Identify the preparation type.
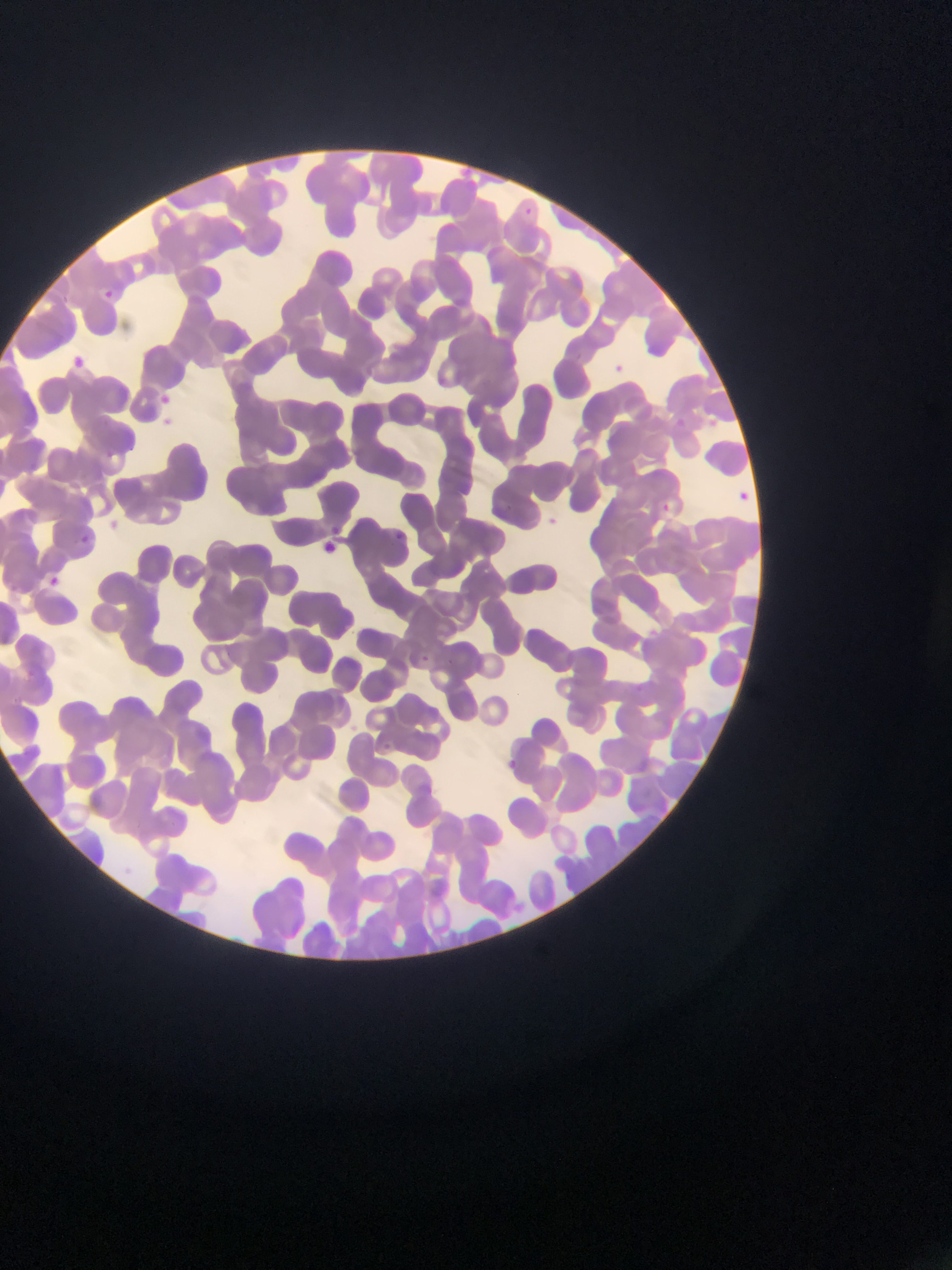

This is a thin smear.

Approximate bounding boxes as (left, top, right, bottom) in pixels.
Summary:
  - Malaria parasite locations: (96, 281, 119, 299), (71, 347, 86, 368), (611, 357, 630, 374), (148, 385, 183, 417), (676, 415, 690, 443), (739, 490, 750, 503), (664, 497, 678, 520), (546, 512, 568, 535), (76, 526, 111, 550), (393, 531, 427, 563), (322, 537, 348, 557), (47, 571, 70, 589), (417, 650, 444, 683), (380, 737, 395, 756), (500, 753, 524, 770)
  - Country: Ghana
  - Image size: 952×1270 pixels
  - Field of view: single
  - Capture: mobile-phone photograph through a microscope